Report the malaria status of this cell.
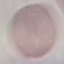

Uninfected.

Summary:
  - Image type: automatically extracted cell patch, resized to 64 × 64 pixels
  - Preparation: thin blood smear
  - Capture: smartphone through the microscope eyepiece
  - Stain: Giemsa